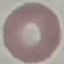

Summary:
  - Result: no malaria parasites detected
  - Image type: cell patch, automatically extracted from a larger field of view and resized to 64 × 64 pixels
  - Stain: Giemsa
  - Capture: smartphone through the microscope eyepiece
  - Preparation: thin blood film